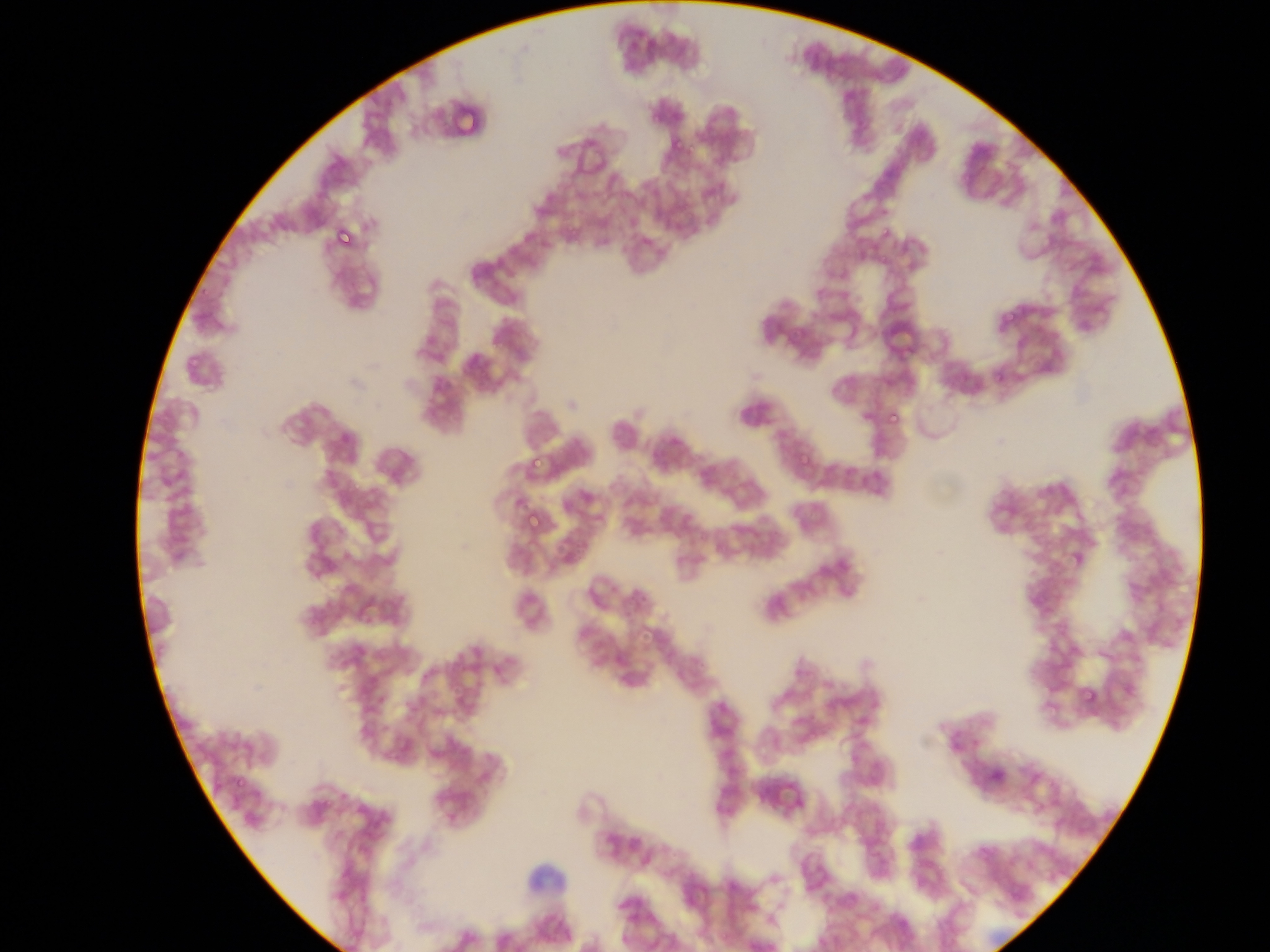 Approximate bounding boxes as (left, top, right, bottom) in pixels. Leukocyte locations: (513, 867, 565, 909). Plasmodium parasite locations: (331, 224, 355, 249), (881, 228, 891, 239), (903, 236, 927, 264), (1002, 312, 1015, 325), (770, 321, 784, 334), (189, 355, 201, 367), (887, 411, 901, 425), (526, 455, 541, 470), (524, 512, 540, 530), (312, 540, 328, 557), (306, 608, 320, 622), (1081, 687, 1098, 705), (395, 734, 412, 752), (231, 777, 245, 791). One field of view. Collected in Ghana. Image is 1270×952 pixels. Thin blood smear. Mobile-phone photograph taken through the microscope.